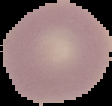
image size = 112×106 pixels
malaria status = uninfected
image type = segmented cell region on a black background
preparation = thin blood film